Assess this cell for malaria.
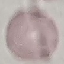

Uninfected.

preparation = thin blood smear
image type = automatically extracted cell patch, resized to 64 × 64 pixels
capture = smartphone through the microscope eyepiece
stain = Giemsa